Assess this cell for malaria.
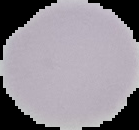
Uninfected.

image type = segmented cell region with the area outside set to black
preparation = thin blood smear
image size = 139×130 pixels